Comment on the morphology of the erythrocytes.
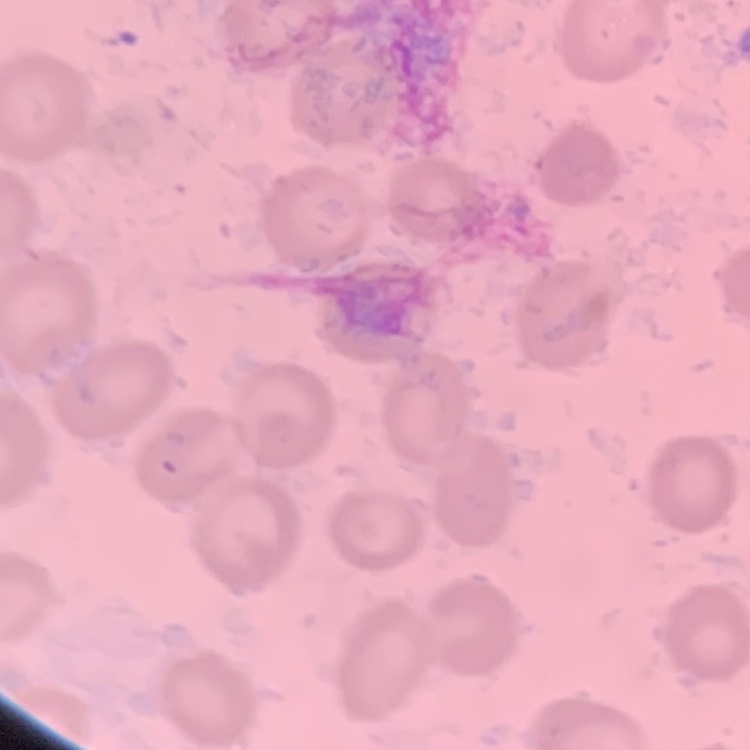
No rouleaux formation.

Summary:
  - Preparation: thin peripheral smear
  - Stain: Field's or Giemsa
  - Image type: one tile cut from a larger photomicrograph